Comment on the morphology of the erythrocytes.
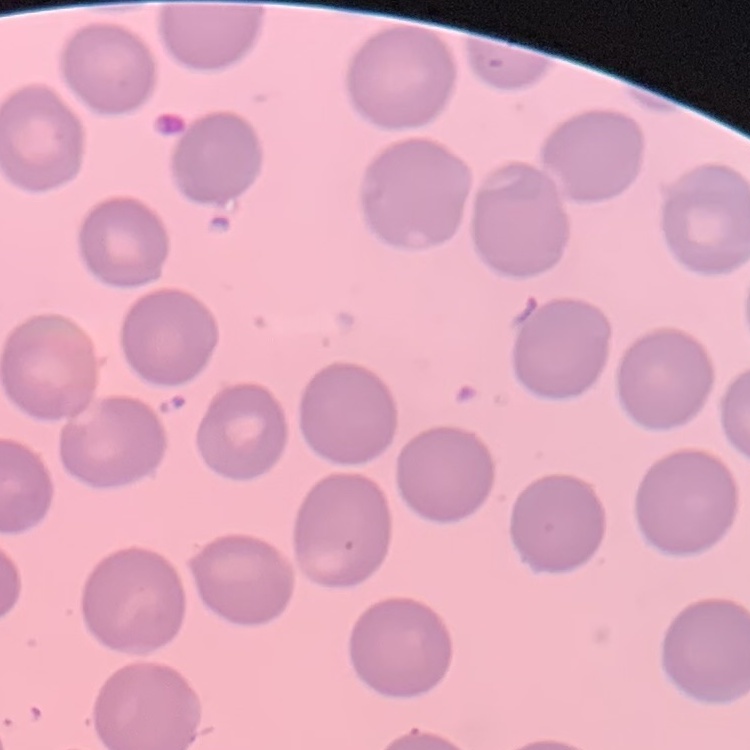

They show no rouleaux formation.

Thin blood film. One tile cut from a larger photomicrograph. Field's or Giemsa stain.